Identify the cell.
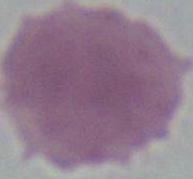

This is an erythrocyte.

Captured at 1000x magnification. Photomicrograph.